Outline each blood parasite and name the species.
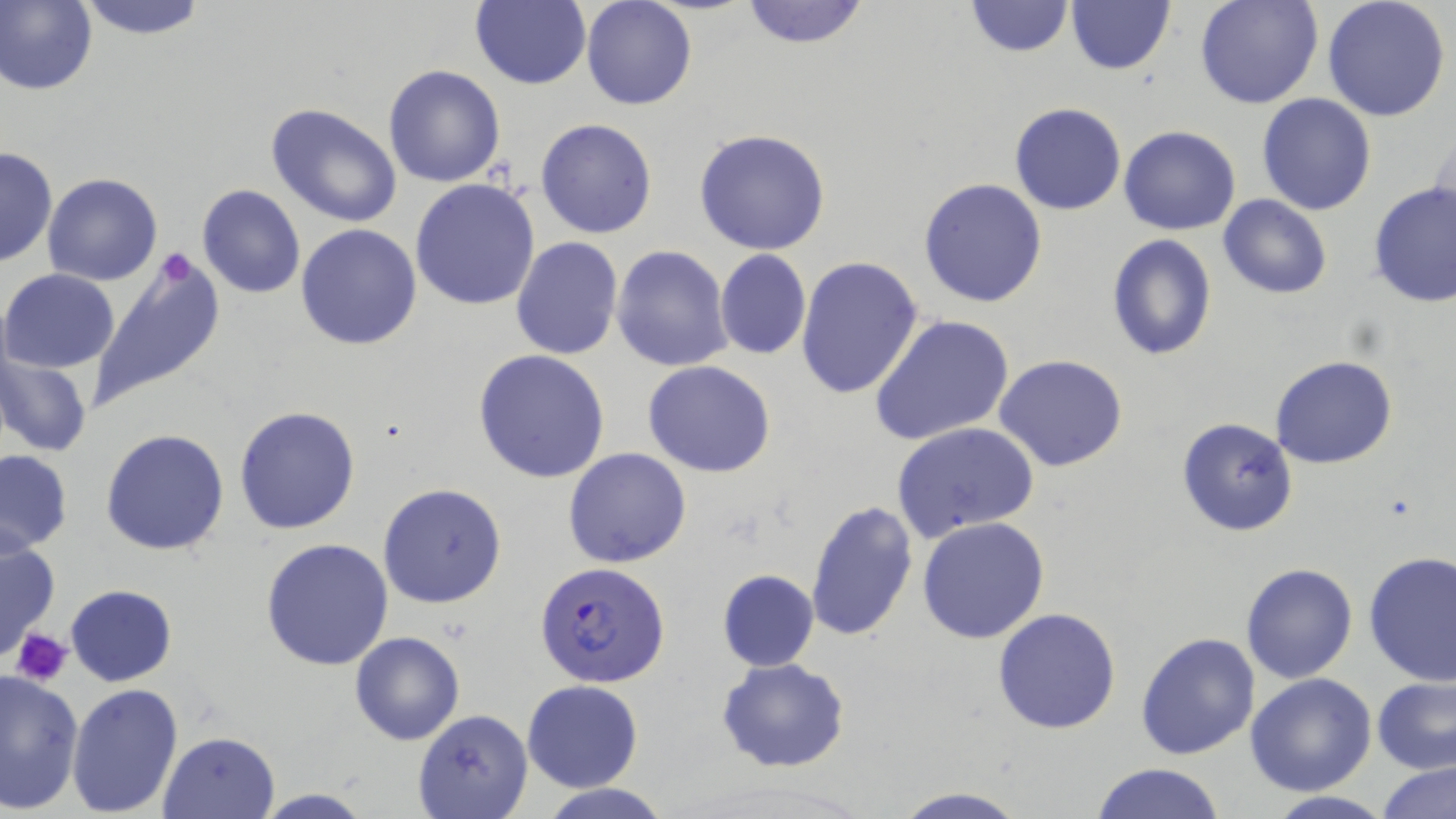
Approximate bounding boxes as [x1, y1, x2, y2] in pixels.
Plasmodium falciparum-infected red blood cells: [535, 561, 670, 689].
No Plasmodium ovale, Plasmodium malariae, Plasmodium vivax, Babesia divergens, or Trypanosoma brucei observed.

slide-level diagnosis = Plasmodium falciparum
magnification = 1000x
image size = 1456×819 pixels
stain = May-Grünwald-Giemsa
field of view = one of a larger specimen
platelet locations = approximate bounding boxes as [x1, y1, x2, y2] in pixels: [159, 252, 201, 284], [12, 630, 71, 689]
preparation = thin blood film
uninfected red blood cell locations = approximate bounding boxes as [x1, y1, x2, y2] in pixels: [0, 0, 97, 95], [69, 0, 214, 39], [581, 0, 698, 110], [737, 0, 871, 49], [1065, 0, 1176, 76], [1195, 0, 1324, 109], [1321, 0, 1451, 122], [468, 1, 591, 89], [965, 1, 1075, 58], [383, 65, 507, 187], [1255, 92, 1377, 216], [264, 101, 406, 229], [1009, 103, 1126, 215], [537, 118, 657, 239], [1119, 125, 1239, 235], [694, 127, 831, 255], [1430, 131, 1455, 235], [1, 146, 57, 267], [43, 173, 162, 287], [917, 177, 1048, 308], [410, 178, 542, 310], [1368, 180, 1456, 306], [197, 185, 306, 299], [1218, 195, 1332, 300], [296, 224, 423, 350], [1105, 233, 1215, 360], [509, 237, 623, 359], [611, 245, 733, 372], [714, 249, 810, 360], [80, 251, 226, 416], [796, 255, 924, 400], [1, 269, 120, 373], [870, 314, 1016, 449], [473, 348, 610, 484], [1, 349, 94, 459], [995, 354, 1129, 474], [1271, 356, 1397, 470], [644, 360, 776, 477], [233, 406, 360, 534], [1175, 416, 1299, 537], [891, 422, 1039, 543], [101, 427, 231, 557], [562, 446, 692, 569], [0, 449, 73, 556], [377, 483, 507, 609], [804, 500, 919, 641], [917, 517, 1051, 645], [0, 534, 59, 660], [260, 537, 395, 671], [1363, 551, 1456, 685], [1241, 562, 1358, 684], [716, 570, 819, 671], [66, 584, 176, 686], [992, 606, 1123, 735], [1135, 631, 1259, 759], [350, 632, 464, 745], [716, 657, 851, 773], [0, 668, 85, 814], [1244, 673, 1376, 796], [1371, 675, 1456, 774], [522, 680, 645, 792], [66, 683, 184, 816], [412, 708, 533, 819], [158, 730, 282, 819], [1089, 761, 1229, 819], [1377, 761, 1456, 819], [537, 784, 674, 819], [888, 785, 1028, 818], [252, 788, 374, 818], [1262, 792, 1395, 819]
modality = optical microscopy